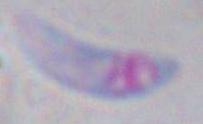

magnification: 1000x
identification: Toxoplasma gondii
modality: photomicrograph